Assess this cell for malaria.
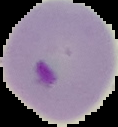

It is parasitized.

The area outside the segmented cell region is set to black. Image is 118×127 pixels. From a thin blood film.